Classify this cell by malaria status.
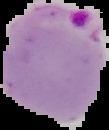

It is parasitized.

preparation = thin blood film
image type = cell region segmented out of the field of view; surrounding area masked to black
image size = 109×130 pixels